Classify this cell by malaria status.
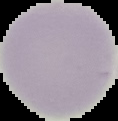

Uninfected.

preparation = thin blood film
image type = cell region segmented out of the field of view; surrounding area masked to black
image size = 118×121 pixels